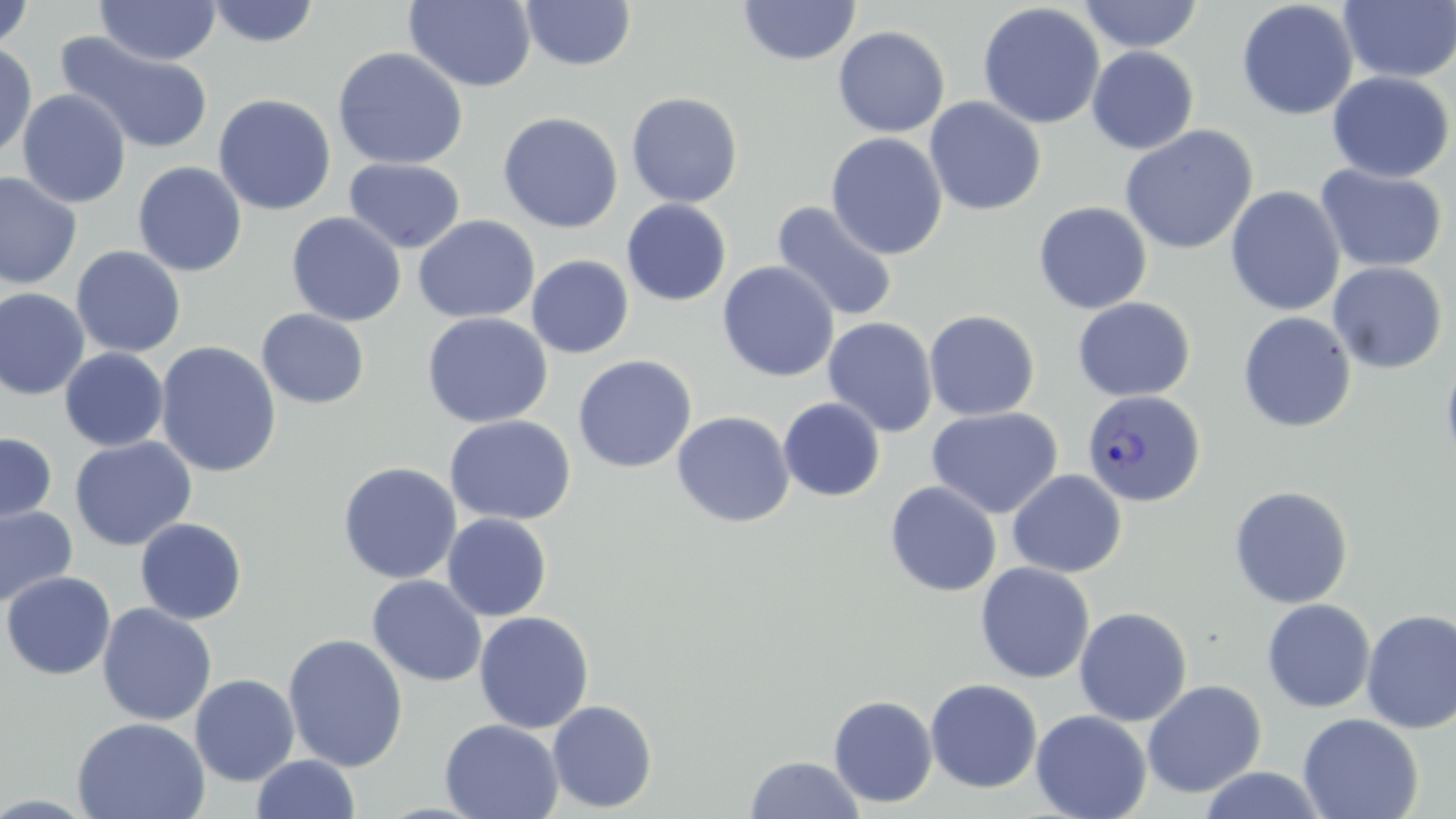
Approximate bounding boxes as (x1,y1)-(x2,y2) corner pairs in pixels. Plasmodium vivax-infected red blood cell locations: (1082,389)-(1205,507). Uninfected red blood cell locations: (403,0)-(538,92), (737,0)-(861,66), (1077,0)-(1204,54), (1236,0)-(1358,121), (1338,0)-(1456,84), (1,1)-(34,52), (95,1)-(222,66), (205,1)-(321,48), (519,1)-(637,71), (977,2)-(1105,130), (832,25)-(951,138), (56,31)-(214,156), (0,43)-(37,162), (331,46)-(469,170), (1086,46)-(1199,154), (1326,71)-(1455,183), (17,89)-(132,208), (626,92)-(744,207), (213,94)-(336,215), (924,97)-(1046,216), (497,112)-(623,234), (1119,125)-(1258,255), (826,132)-(948,260), (343,157)-(466,254), (132,161)-(247,277), (1315,164)-(1448,273), (0,172)-(83,289), (1225,186)-(1345,316), (621,199)-(732,307), (771,201)-(899,324), (1033,201)-(1152,315), (286,212)-(407,327), (412,215)-(540,324), (71,245)-(186,358), (526,255)-(634,359), (717,261)-(839,382), (1328,261)-(1448,374), (0,288)-(90,399), (1072,297)-(1195,402), (256,309)-(370,410), (923,310)-(1040,421), (1237,311)-(1357,433), (420,312)-(554,429), (822,317)-(938,437), (155,342)-(280,479), (59,348)-(169,451), (1440,349)-(1456,471), (572,354)-(697,473), (778,397)-(886,502), (926,406)-(1063,520), (671,410)-(795,528), (444,415)-(576,525), (0,432)-(57,526), (69,436)-(197,551), (338,461)-(462,584), (1007,469)-(1127,578), (884,480)-(1002,597), (1229,485)-(1353,608), (0,504)-(77,609), (442,513)-(552,621), (135,517)-(247,625), (974,562)-(1095,683), (2,570)-(116,680), (367,574)-(487,687), (1261,599)-(1375,713), (96,603)-(217,726), (1074,606)-(1193,727), (1360,609)-(1456,734), (474,611)-(594,734), (283,633)-(409,772), (189,674)-(300,786), (925,678)-(1043,793), (1142,679)-(1267,798), (828,695)-(938,808), (547,699)-(658,813), (1030,709)-(1152,819), (1298,713)-(1423,819), (72,716)-(211,819), (439,718)-(564,819), (252,753)-(361,819), (745,754)-(866,818), (1198,767)-(1329,819). Slide-level diagnosis: Plasmodium vivax. One field of a larger specimen. Light microscopy. 1000x magnification. Thin blood smear. May-Grünwald-Giemsa stain. Image is 1456×819 pixels.